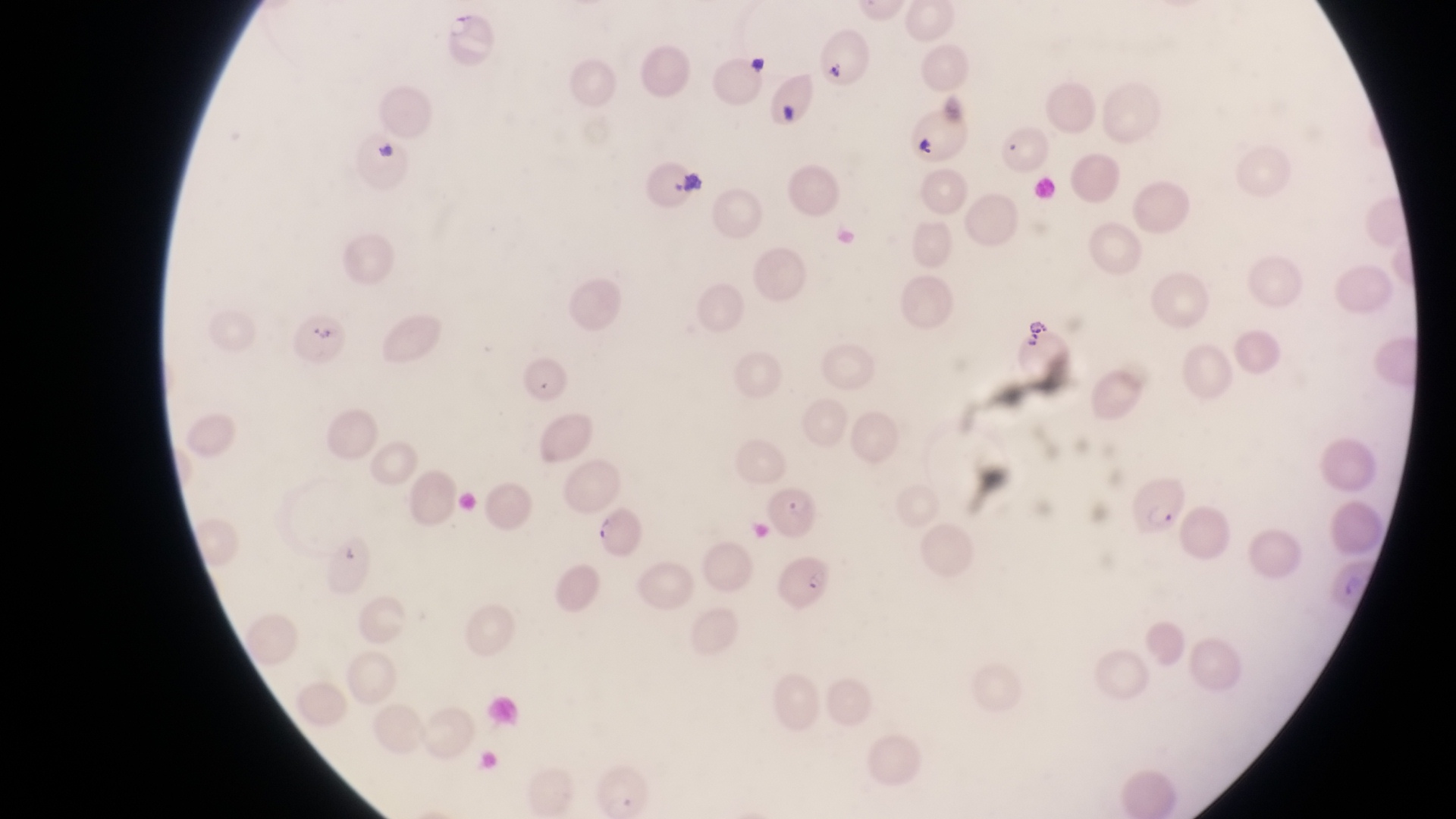

Approximate bounding boxes as (left, top, right, bottom) in pixels.
Summary:
  - Artifact (platelet-like body, stain precipitate, or debris) locations: (827, 58, 851, 85), (777, 102, 800, 123), (679, 168, 711, 196), (310, 327, 342, 347)
  - Parasitised red blood cell locations: (908, 111, 967, 163), (1018, 331, 1073, 383), (766, 486, 822, 532), (595, 508, 647, 560), (780, 554, 835, 613)
  - Image size: 1456×819 pixels
  - Preparation: thin blood smear
  - Field of view: single
  - Capture: smartphone photograph through the eyepiece of an Olympus CX-23 microscope
  - Country: Uganda
  - Magnification: 1000x